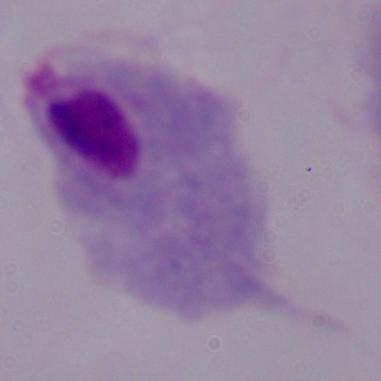

Summary:
  - Modality: photomicrograph
  - Identification: trichomonad
  - Magnification: 1000x